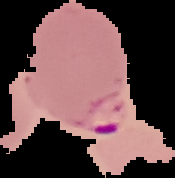

image_size: 175×178 pixels
preparation: thin blood film
image_type: cell region segmented out of the field of view; surrounding area masked to black
result: malaria parasites identified